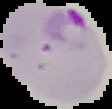
From a thin blood smear. Malaria status: parasitized. Image is 112×109 pixels. The area outside the segmented cell region is set to black.